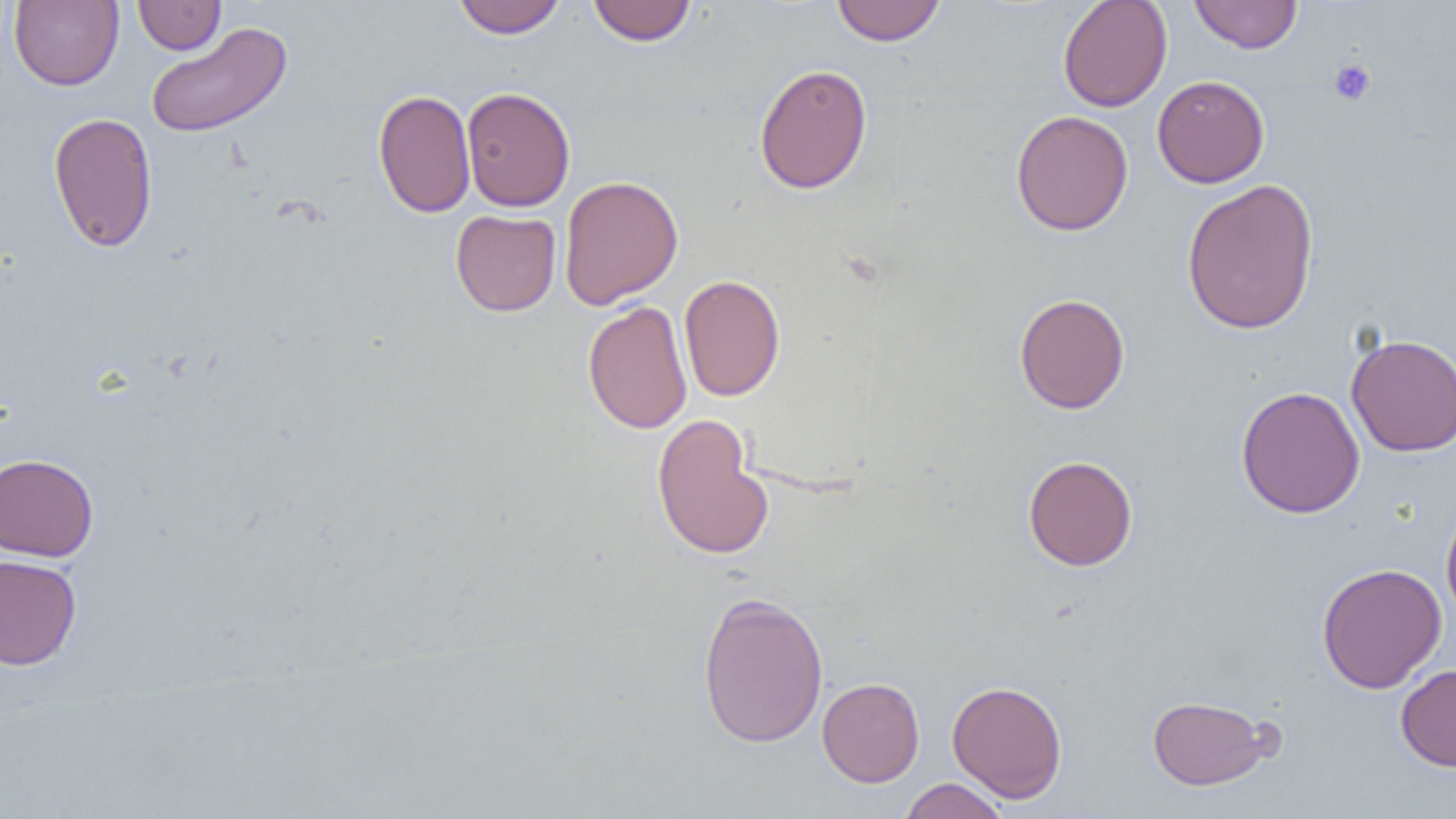
Approximate bounding boxes as (x1,y1)-(x2,y2) corner pairs in pixels. Uninfected red blood cell locations: (9,0)-(124,90), (132,0)-(226,55), (452,0)-(566,38), (587,0)-(697,46), (831,0)-(945,46), (1057,0)-(1172,112), (1188,0)-(1303,54), (145,21)-(292,139), (754,62)-(872,195), (1152,74)-(1270,188), (461,86)-(576,212), (373,88)-(476,218), (1011,109)-(1134,236), (47,111)-(158,252), (559,174)-(683,310), (1181,177)-(1320,335), (450,209)-(561,316), (679,274)-(785,401), (1014,293)-(1130,414), (583,300)-(693,434), (1346,333)-(1456,457), (1235,386)-(1365,518), (651,413)-(774,561), (0,453)-(99,561), (1023,455)-(1138,571), (1441,499)-(1456,625), (0,554)-(82,670), (1317,562)-(1447,693), (697,591)-(829,748), (1396,664)-(1456,772), (817,677)-(924,787), (947,679)-(1067,803), (1146,694)-(1277,790), (898,778)-(1011,819). Platelet locations: (1329,59)-(1376,106). Slide-level diagnosis: no evidence of blood parasites. Captured at 1000x magnification. One field of a larger specimen. Image is 1456×819 pixels. Optical microscopy. Thin blood film.